State which parasite is depicted.
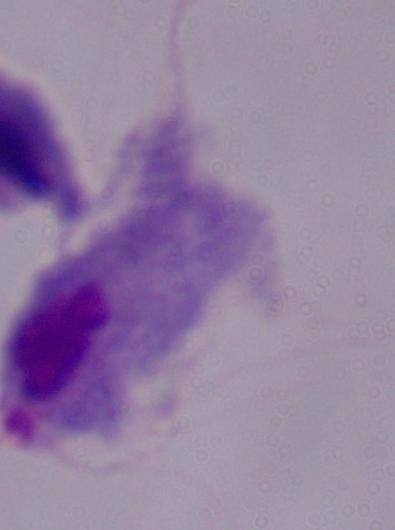

This is a trichomonad.

Summary:
  - Magnification: 1000x
  - Modality: micrograph